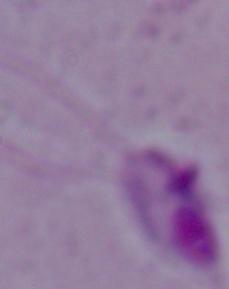

Summary:
  - Modality: photomicrograph
  - Identification: Leishmania
  - Magnification: 1000x